Classify this cell by malaria status.
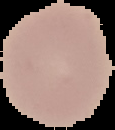

It is uninfected.

preparation = thin blood smear
image type = cell region segmented out of the field of view; surrounding area masked to black
image size = 115×130 pixels